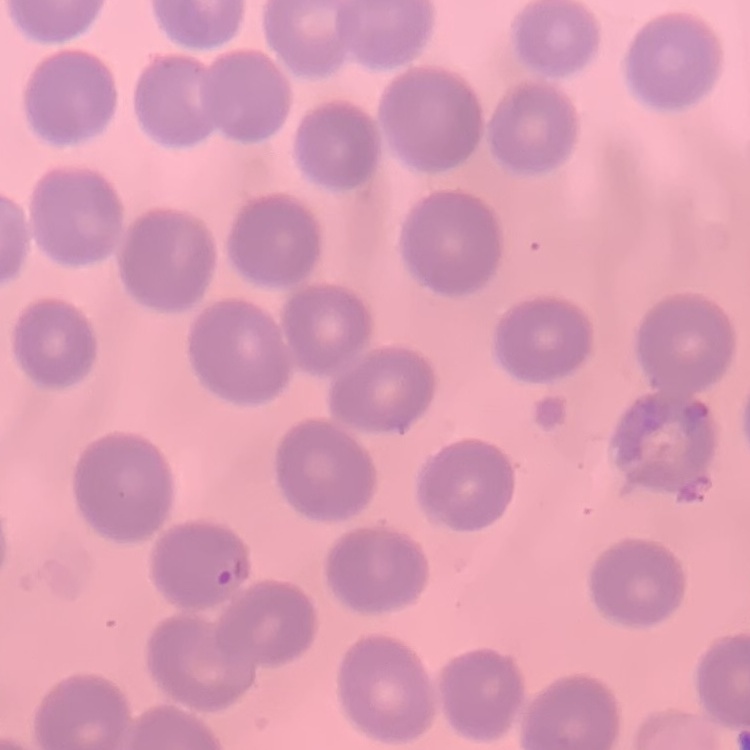

Summary:
  - Red blood cell morphology: no rouleaux formation
  - Image type: square crop of a larger photomicrograph
  - Preparation: thin blood smear
  - Stain: Field's or Giemsa